Give the position of every Plasmodium parasite visible.
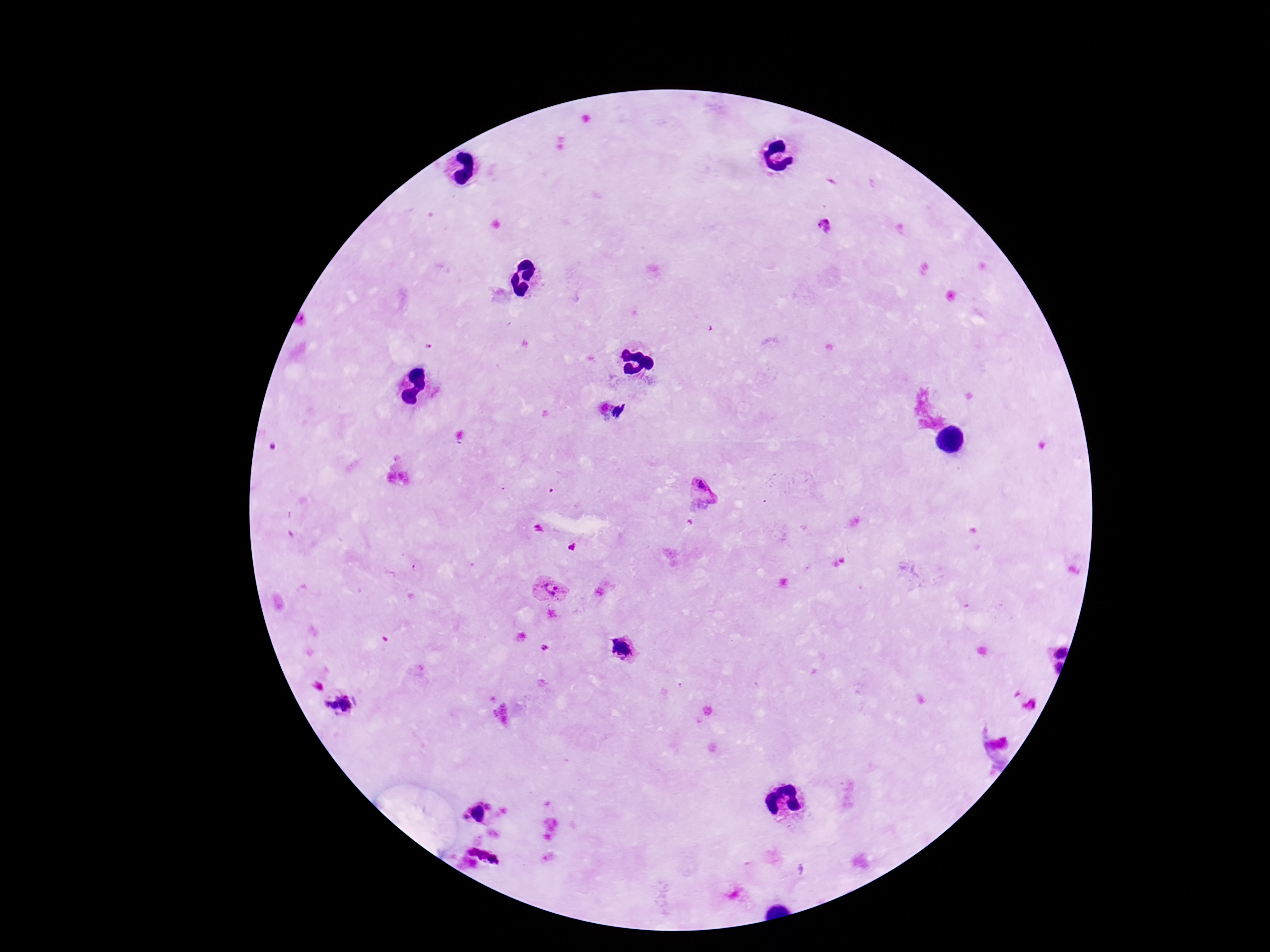

Approximate centers as [x, y] in pixels.
Plasmodium parasites: [826, 227], [705, 487], [552, 589], [601, 592], [546, 647], [622, 648], [1061, 651], [1056, 669], [341, 703], [478, 813], [485, 855].

patient_malaria_status: infected
field_of_view: one from this slide
capture: smartphone camera through the microscope eyepiece
image_size: 1270×952 pixels
preparation: thick blood film
magnification: 100x
stain: Giemsa